Classify this cell by malaria status.
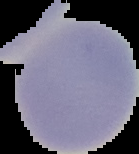

Uninfected.

Summary:
  - Preparation: thin blood film
  - Image size: 139×154 pixels
  - Image type: cell region segmented out of the field of view; surrounding area masked to black